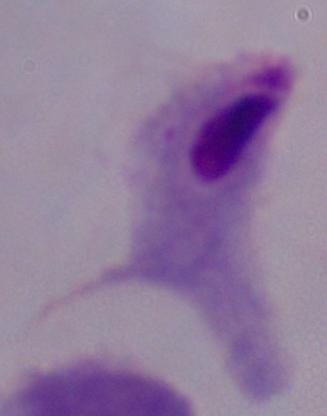

identification = trichomonad
magnification = 1000x
modality = micrograph